Describe the morphology of the erythrocytes.
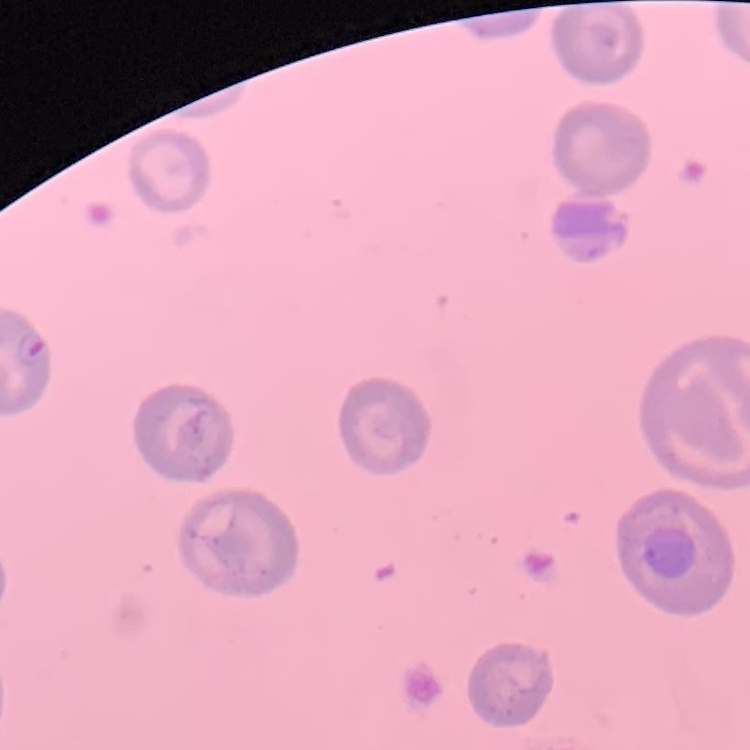
They show no rouleaux formation.

Stained with either Field's or Giemsa. Square crop of a larger photomicrograph. Thin blood smear.